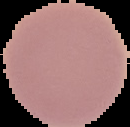
{
  "result": "negative for malaria parasites",
  "preparation": "thin blood film",
  "image_size": "130×127 pixels",
  "image_type": "segmented cell region with the area outside set to black"
}